Report the malaria status.
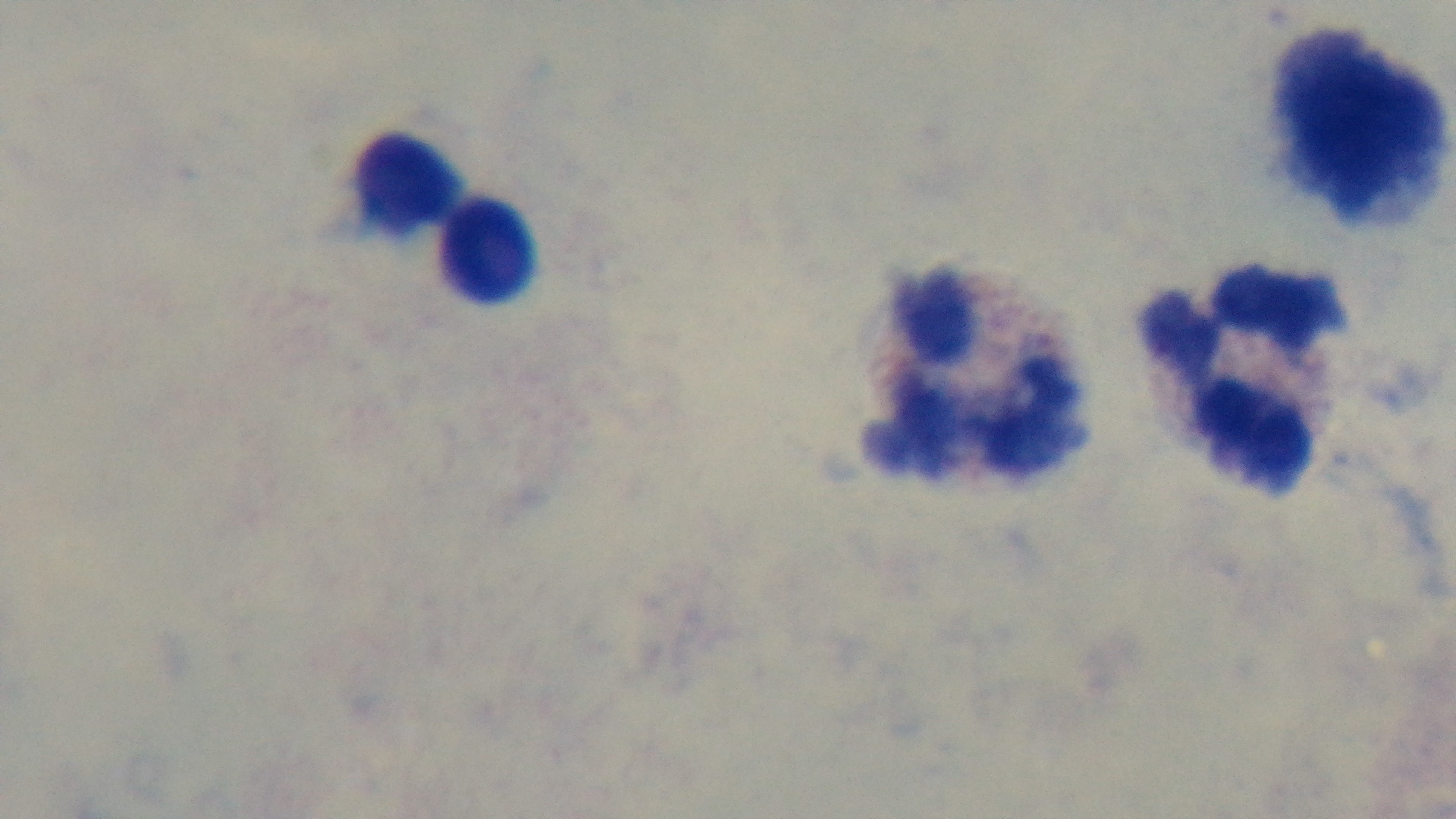
It is uninfected.

Summary:
  - Stain: Giemsa
  - Preparation: thick
  - Field of view: one from the slide
  - Objective: 100x oil immersion
  - Modality: light microscopy
  - Capture: mounted 4K digital camera